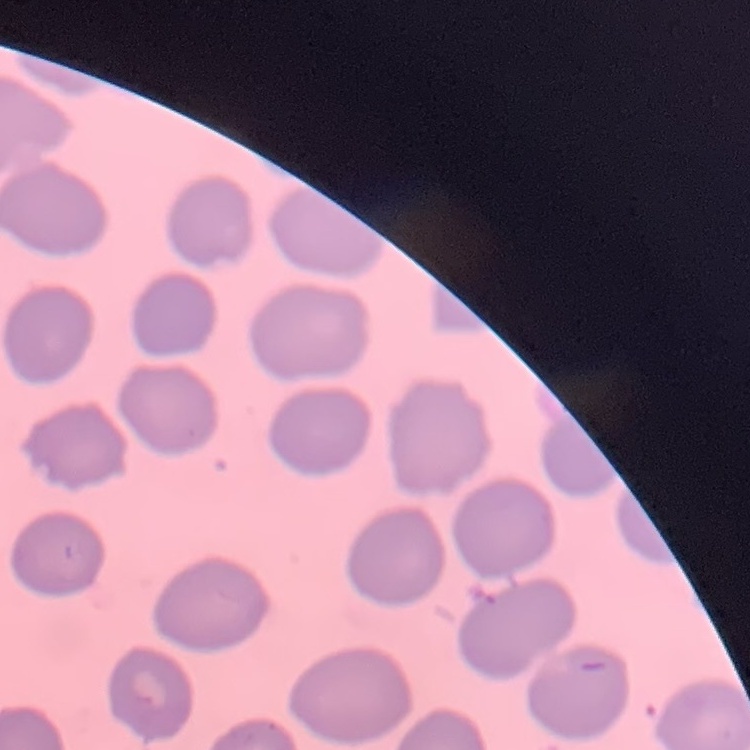
Summary:
  - Red blood cell morphology: no rouleaux formation
  - Preparation: thin blood smear
  - Image type: square crop of a larger photomicrograph
  - Stain: Field's or Giemsa